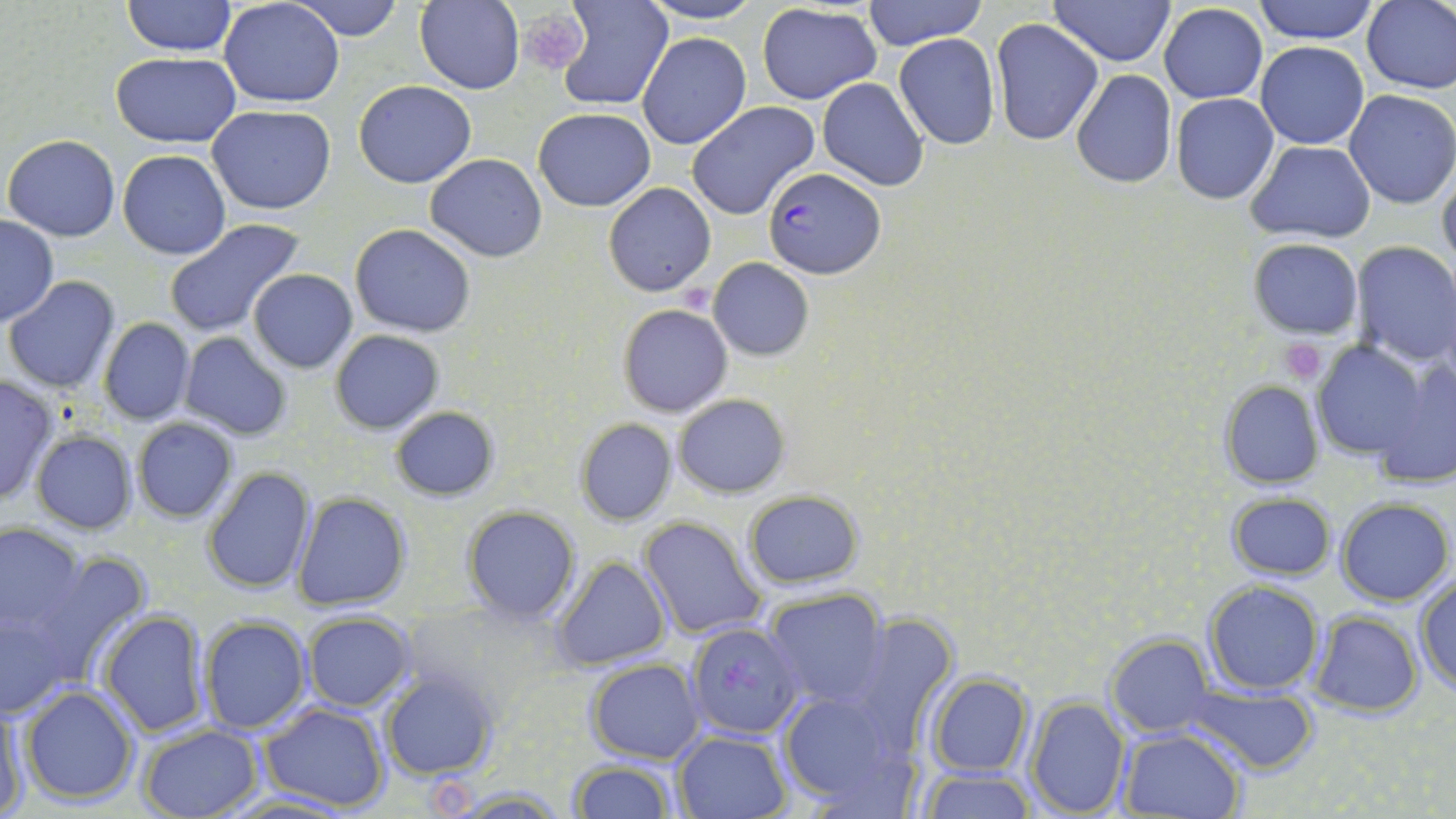

Summary:
  - Coordinate format: approximate bounding boxes as (x1,y1)-(x2,y2) corner pairs in pixels
  - Uninfected red blood cell locations: (124,0)-(235,55), (219,0)-(345,108), (288,0)-(404,41), (552,0)-(673,112), (637,0)-(766,26), (863,0)-(987,51), (1050,0)-(1174,65), (1253,0)-(1382,44), (1361,0)-(1456,94), (414,1)-(526,94), (1158,3)-(1267,104), (757,4)-(881,104), (990,18)-(1105,147), (639,33)-(751,150), (894,34)-(1000,149), (1257,42)-(1369,149), (111,53)-(241,146), (1070,69)-(1177,189), (818,78)-(929,191), (354,81)-(476,187), (1345,90)-(1456,209), (1170,92)-(1279,205), (685,101)-(821,219), (207,105)-(336,214), (534,109)-(654,211), (5,134)-(120,240), (1248,142)-(1377,243), (118,150)-(232,259), (424,154)-(548,260), (1437,168)-(1456,271), (604,184)-(715,296), (0,216)-(59,326), (163,218)-(304,337), (350,224)-(476,336), (1248,237)-(1362,339), (1351,240)-(1456,367), (708,258)-(814,361), (247,269)-(357,373), (5,276)-(122,392), (618,304)-(734,417), (98,318)-(196,425), (330,330)-(444,434), (179,331)-(294,442), (1309,340)-(1429,468), (1374,359)-(1456,489), (0,375)-(59,505), (1220,381)-(1324,490), (672,393)-(791,497), (389,405)-(500,501), (132,418)-(237,523), (574,418)-(677,526), (31,429)-(136,533), (203,465)-(316,595), (742,489)-(862,589), (293,492)-(411,610), (1226,493)-(1336,581), (1336,498)-(1453,604), (461,504)-(581,625), (638,515)-(768,642), (0,522)-(86,633), (22,552)-(151,686), (554,557)-(669,671), (1414,576)-(1456,694), (1203,580)-(1325,696), (765,589)-(889,709), (0,597)-(80,717), (97,609)-(210,737), (1307,610)-(1424,717), (302,611)-(417,711), (840,614)-(959,750), (198,615)-(309,735), (1106,634)-(1214,736), (586,659)-(707,765), (381,671)-(497,780), (926,674)-(1032,776), (20,684)-(139,806), (1186,685)-(1319,773), (776,689)-(917,815), (0,696)-(29,818), (1024,697)-(1131,818), (259,703)-(390,814), (138,723)-(263,818), (1117,727)-(1247,818), (673,731)-(790,819), (568,758)-(676,818), (918,767)-(1037,819), (442,785)-(573,817), (223,791)-(356,819)
  - Platelet locations: (515,11)-(589,76), (1278,338)-(1327,383)
  - Plasmodium falciparum-infected red blood cell locations: (760,165)-(886,279), (686,620)-(803,739)
  - Slide-level diagnosis: Plasmodium falciparum
  - Magnification: 1000x
  - Field of view: one of a larger specimen
  - Stain: May-Grünwald-Giemsa
  - Preparation: thin blood film
  - Image size: 1456×819 pixels
  - Modality: light microscopy